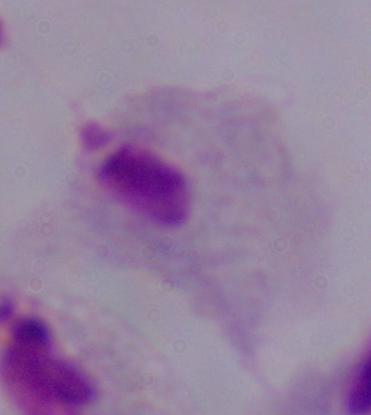

modality: photomicrograph
magnification: 1000x
identification: trichomonad